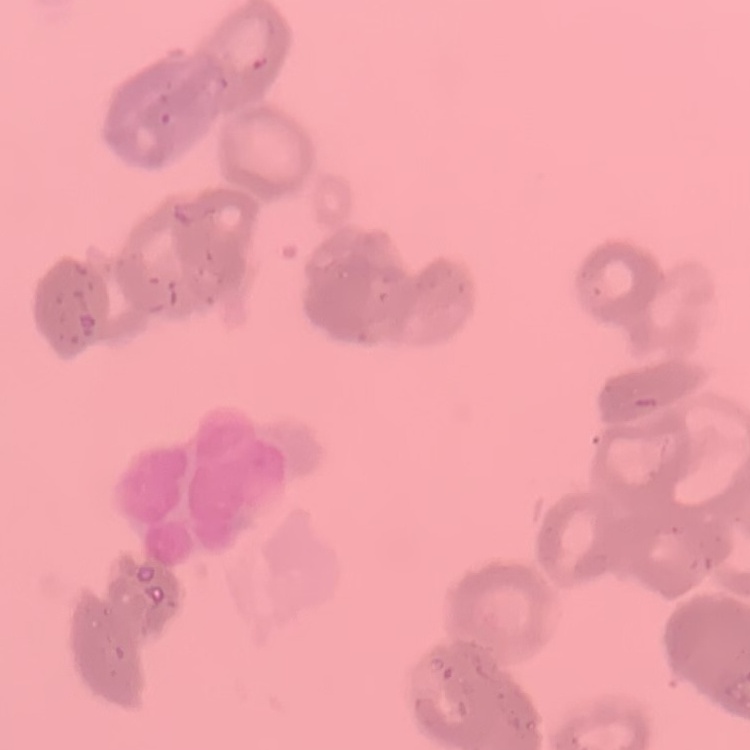
Summary:
  - Red blood cell morphology: rouleaux formation
  - Image type: one tile cut from a larger photomicrograph
  - Stain: Field's or Giemsa
  - Preparation: thin blood smear